Assess for malaria.
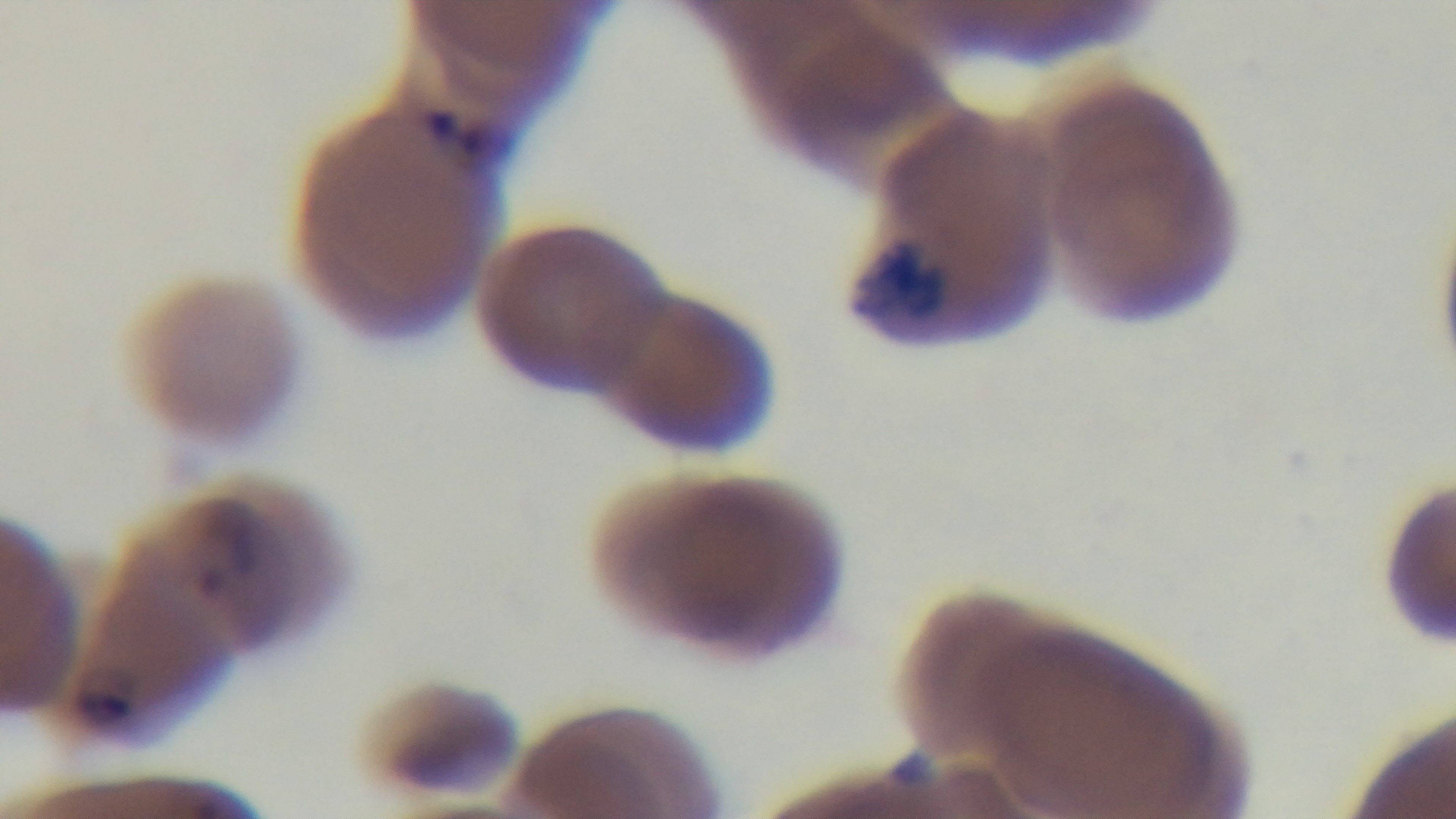
It is infected.

Giemsa-stained. Captured with a mounted 4K digital camera. Preparation: thin blood film. Light microscopy. Single field of view. Oil-immersion objective, 100x.